Identify the blood parasite species.
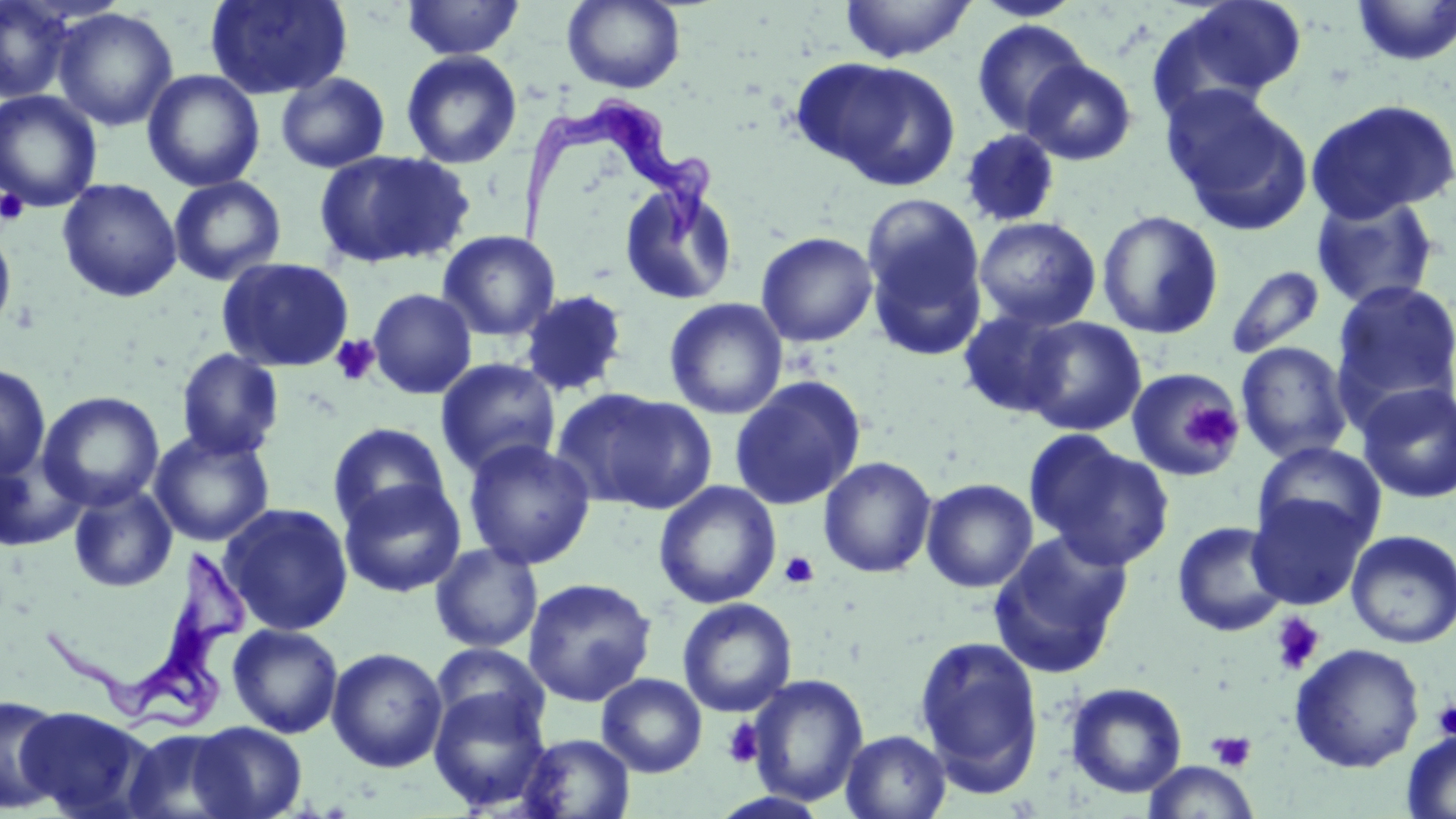

Trypanosoma brucei.

Summary:
  - Coordinate format: approximate bounding boxes as (x1, y1, x2, y2) in pixels
  - Uninfected red blood cell locations: (0, 0, 75, 104), (205, 0, 353, 100), (402, 0, 525, 60), (562, 0, 686, 93), (839, 0, 976, 63), (970, 0, 1084, 22), (1159, 0, 1309, 106), (1350, 0, 1456, 68), (52, 8, 179, 132), (971, 19, 1093, 138), (401, 50, 522, 169), (793, 56, 961, 191), (1021, 58, 1138, 165), (142, 69, 265, 191), (275, 72, 390, 174), (1162, 85, 1313, 236), (0, 90, 103, 212), (1304, 98, 1456, 223), (959, 128, 1062, 227), (314, 150, 474, 270), (167, 175, 286, 286), (57, 178, 182, 302), (619, 178, 739, 306), (1310, 193, 1441, 311), (861, 194, 990, 361), (1096, 210, 1224, 340), (973, 216, 1100, 331), (0, 224, 17, 337), (438, 231, 560, 342), (756, 231, 878, 347), (217, 257, 355, 372), (1225, 265, 1326, 359), (1331, 281, 1456, 413), (367, 288, 477, 399), (519, 289, 629, 398), (664, 297, 788, 420), (957, 306, 1079, 419), (1018, 316, 1147, 436), (1235, 341, 1353, 464), (176, 349, 284, 460), (435, 358, 561, 480), (0, 364, 51, 480), (1126, 368, 1244, 481), (729, 375, 866, 511), (1356, 382, 1456, 504), (553, 388, 717, 515), (38, 391, 165, 512), (327, 422, 451, 532), (149, 429, 276, 547), (1026, 434, 1174, 571), (463, 439, 596, 570), (1252, 442, 1386, 551), (0, 451, 87, 551), (818, 456, 937, 578), (338, 478, 467, 597), (921, 478, 1038, 593), (653, 481, 781, 609), (68, 483, 178, 593), (1246, 491, 1371, 611), (220, 502, 354, 636), (1172, 520, 1290, 637), (1346, 529, 1456, 649), (988, 530, 1133, 679), (430, 543, 544, 653), (523, 577, 657, 707), (677, 598, 797, 717), (227, 623, 343, 738), (912, 634, 1045, 794), (431, 643, 549, 740), (1290, 643, 1425, 773), (327, 647, 448, 773), (597, 673, 708, 777), (747, 674, 869, 806), (1065, 681, 1187, 798), (428, 687, 551, 812), (0, 694, 66, 814), (18, 705, 155, 819), (188, 721, 307, 818), (121, 727, 244, 819), (841, 730, 951, 819), (1401, 730, 1456, 819), (518, 733, 635, 818), (1142, 761, 1258, 819)
  - Platelet locations: (0, 188, 28, 225), (330, 335, 380, 386), (1183, 400, 1245, 458), (779, 552, 820, 588), (1270, 613, 1326, 676), (1431, 698, 1456, 741), (722, 718, 765, 769), (1207, 730, 1257, 772)
  - Trypanosoma brucei locations: (512, 93, 720, 254), (39, 546, 253, 738)
  - Image size: 1456×819 pixels
  - Modality: optical microscopy
  - Preparation: thin blood film
  - Stain: May-Grünwald-Giemsa
  - Field of view: single
  - Magnification: 1000x